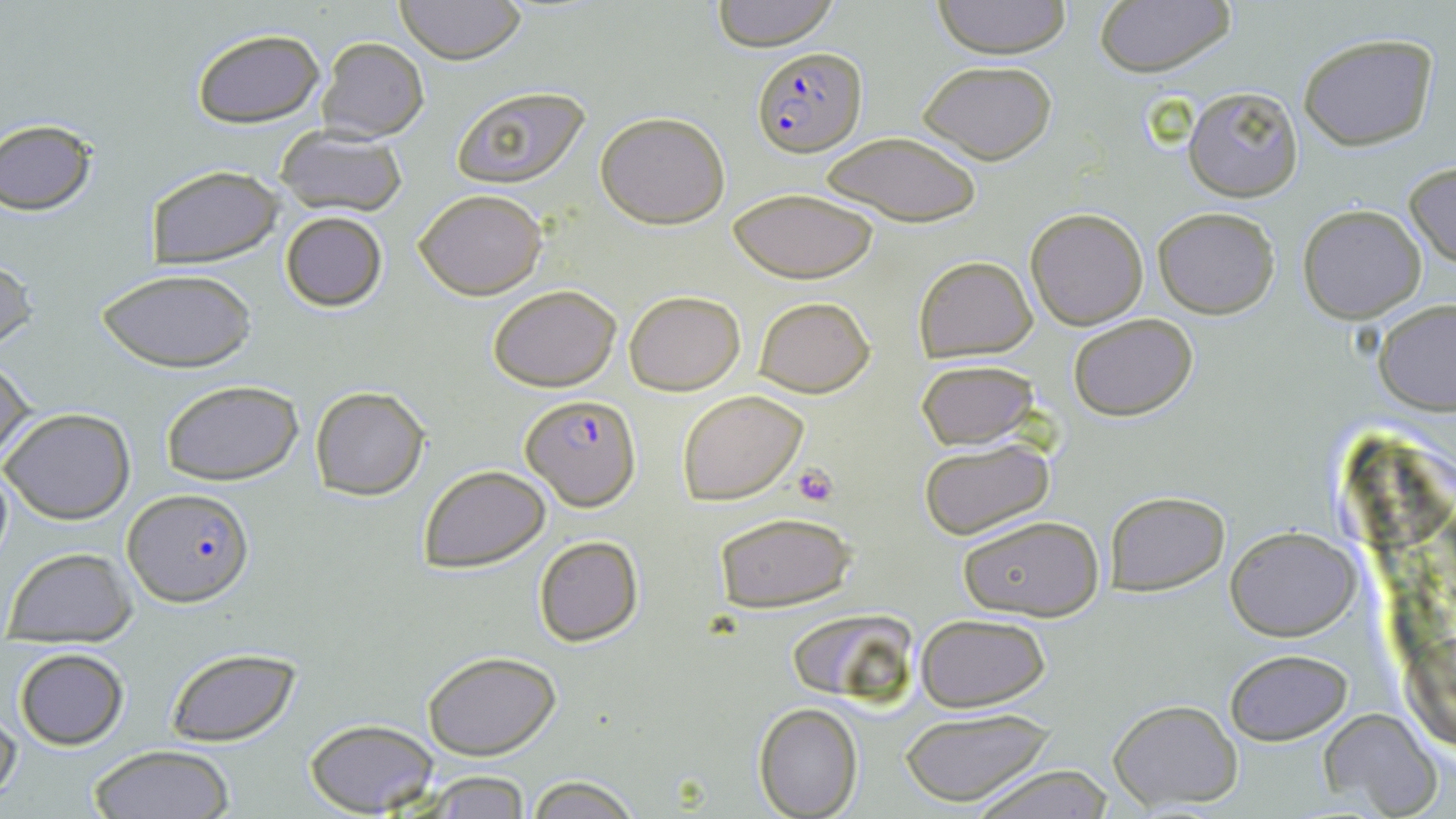
slide-level diagnosis = Plasmodium falciparum
magnification = 1000x
platelet locations = approximate bounding boxes as [x1, y1, x2, y2] in pixels: [791, 463, 841, 507]
modality = optical microscopy
image size = 1456×819 pixels
preparation = thin blood film
uninfected red blood cell locations = approximate bounding boxes as [x1, y1, x2, y2] in pixels: [394, 0, 527, 65], [709, 0, 840, 50], [932, 0, 1073, 58], [1093, 0, 1237, 76], [191, 29, 323, 128], [1298, 32, 1440, 151], [318, 37, 429, 144], [917, 60, 1059, 165], [449, 83, 594, 190], [1184, 86, 1303, 202], [596, 111, 730, 227], [0, 119, 99, 215], [275, 127, 408, 217], [818, 130, 982, 226], [1403, 161, 1456, 270], [144, 165, 282, 267], [727, 187, 880, 283], [414, 188, 547, 299], [1297, 204, 1426, 322], [1025, 206, 1149, 330], [1152, 207, 1280, 318], [280, 212, 388, 311], [913, 255, 1037, 362], [0, 258, 36, 356], [97, 268, 257, 374], [489, 284, 622, 391], [623, 289, 746, 395], [752, 296, 875, 398], [1376, 300, 1456, 415], [1067, 313, 1199, 422], [0, 355, 36, 468], [914, 360, 1040, 452], [160, 381, 304, 486], [310, 385, 431, 499], [677, 389, 808, 504], [2, 408, 134, 525], [916, 437, 1060, 543], [0, 458, 14, 571], [418, 464, 551, 571], [1104, 490, 1231, 597], [712, 510, 857, 613], [958, 513, 1104, 621], [1226, 528, 1361, 640], [533, 534, 644, 646], [3, 546, 137, 643], [783, 607, 916, 708], [914, 612, 1052, 712], [12, 647, 128, 749], [163, 648, 302, 747], [1224, 649, 1351, 745], [422, 650, 562, 759], [1107, 698, 1244, 808], [753, 702, 862, 818], [896, 705, 1055, 806], [0, 706, 21, 806], [1320, 709, 1448, 819], [304, 718, 440, 817], [89, 745, 237, 819], [963, 764, 1119, 818], [416, 771, 533, 817], [525, 775, 643, 818]
field of view = single
stain = May-Grünwald-Giemsa
Plasmodium falciparum-infected red blood cell locations = approximate bounding boxes as [x1, y1, x2, y2] in pixels: [751, 44, 867, 155], [521, 397, 639, 510], [125, 488, 254, 605]